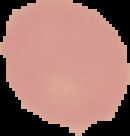

Malaria status: uninfected. From a thin blood smear. Image is 130×136 pixels. Cell region segmented out of the field of view; the surrounding area is masked to black.